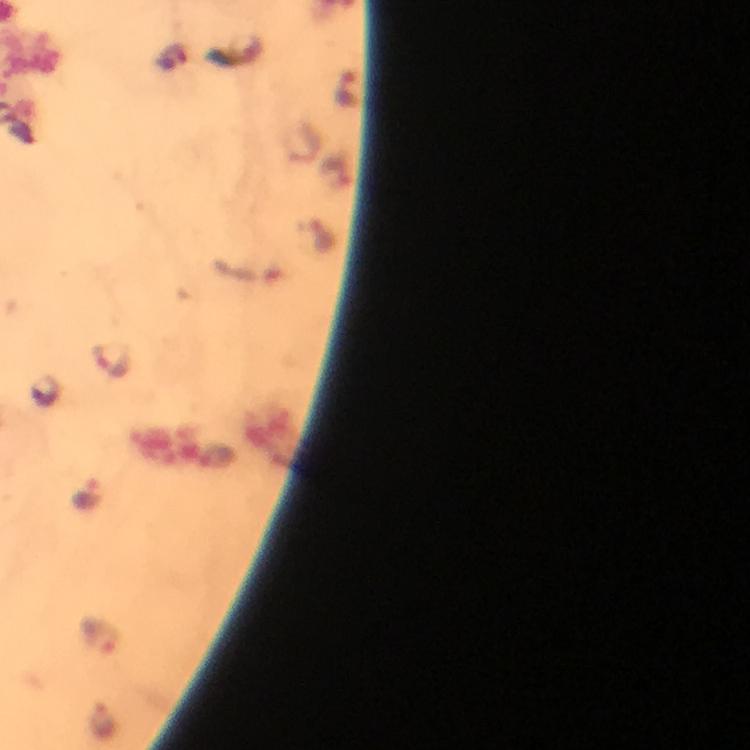
Approximate centers as {x, y} in pixels. Plasmodium parasite locations: {111, 362}, {89, 494}, {99, 636}. Image is 750×750 pixels. Giemsa-stained preparation. From a malaria diagnostic workup. Cropped region of a single field of view. 100x magnification. Thick blood smear. Photographed with a smartphone mounted on the microscope. Immersion oil applied.